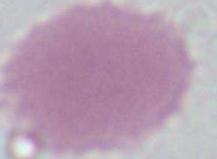

modality: micrograph
identification: red blood cell
magnification: 1000x